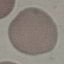
malaria status = uninfected
preparation = thin smear
capture = smartphone through the microscope eyepiece
stain = Giemsa
image type = automatically extracted cell patch, resized to 64 × 64 pixels